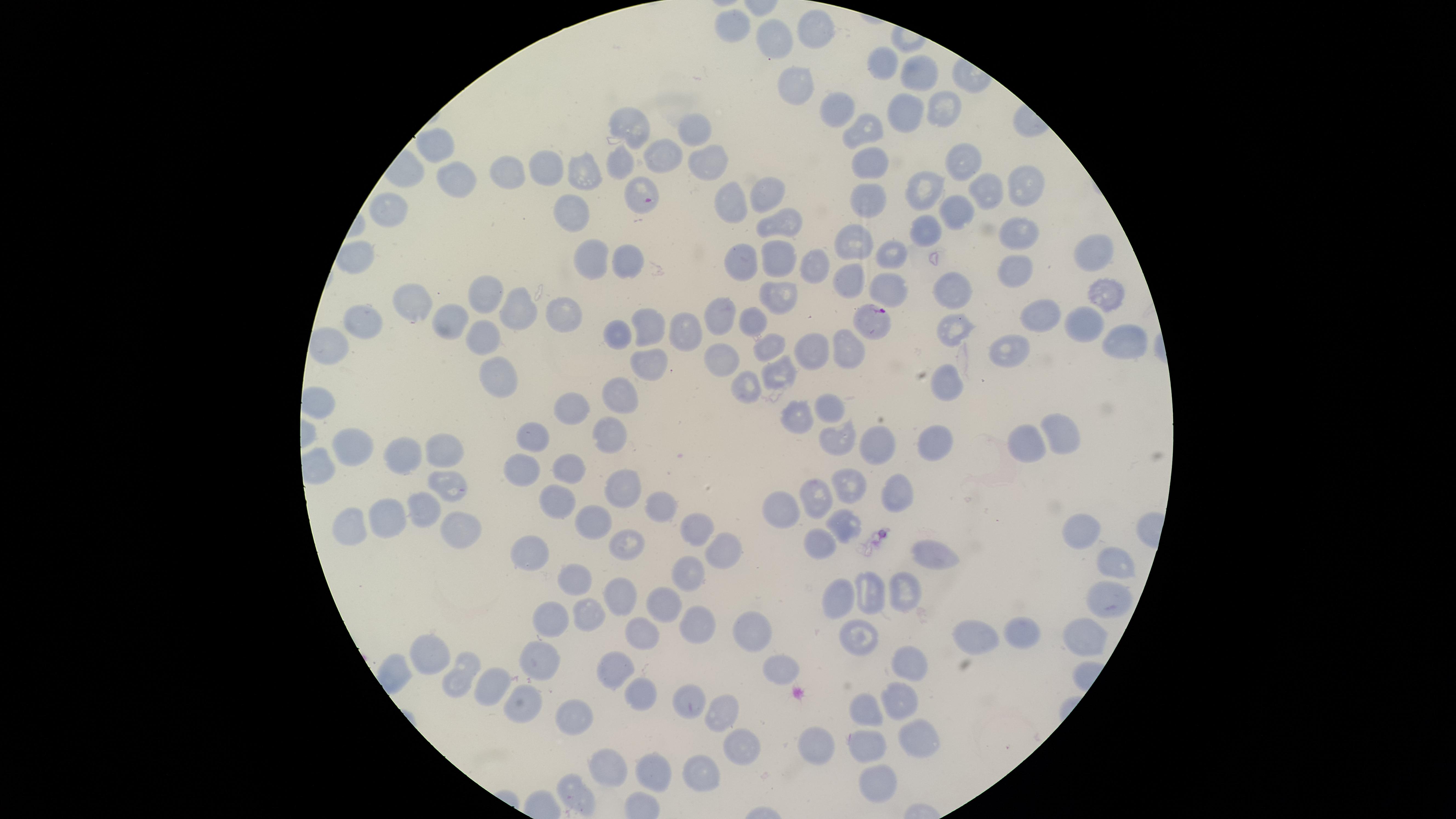

Approximate marker points, in pixels from the top-left corner.
Summary:
  - Parasitized red blood cells: (x=641, y=191), (x=877, y=320)
  - Uninfected red blood cells: (x=735, y=23), (x=813, y=27), (x=776, y=38), (x=884, y=60), (x=922, y=73), (x=797, y=87), (x=909, y=106), (x=840, y=107), (x=946, y=107), (x=632, y=124), (x=867, y=126), (x=692, y=129), (x=431, y=145), (x=666, y=155), (x=967, y=159), (x=707, y=160), (x=873, y=163), (x=622, y=164), (x=546, y=169), (x=583, y=169), (x=506, y=172), (x=446, y=176), (x=1028, y=178), (x=922, y=186), (x=768, y=188), (x=982, y=192), (x=732, y=197), (x=867, y=199), (x=386, y=208), (x=956, y=210), (x=570, y=211), (x=785, y=222), (x=926, y=226), (x=1017, y=229), (x=856, y=241), (x=1091, y=248), (x=779, y=254), (x=892, y=254), (x=590, y=255), (x=748, y=258), (x=814, y=259), (x=624, y=262), (x=1016, y=266), (x=849, y=279), (x=891, y=286), (x=951, y=287), (x=1107, y=287), (x=484, y=290), (x=783, y=294), (x=413, y=300), (x=513, y=305), (x=562, y=313), (x=1036, y=315), (x=363, y=319), (x=1077, y=319), (x=722, y=320), (x=447, y=321), (x=755, y=323), (x=951, y=324), (x=648, y=325), (x=486, y=331), (x=616, y=333), (x=683, y=334), (x=1119, y=334), (x=1005, y=342), (x=775, y=343), (x=808, y=344), (x=853, y=352), (x=722, y=355), (x=653, y=363), (x=497, y=370), (x=777, y=371), (x=741, y=382), (x=949, y=384), (x=620, y=397), (x=577, y=406), (x=828, y=409), (x=796, y=415), (x=1063, y=427), (x=614, y=433), (x=1024, y=437), (x=536, y=439), (x=840, y=439), (x=880, y=441), (x=932, y=441), (x=357, y=445), (x=446, y=450), (x=407, y=452), (x=568, y=463), (x=521, y=466), (x=447, y=485), (x=621, y=485), (x=851, y=485), (x=895, y=493), (x=559, y=497), (x=814, y=499), (x=660, y=502), (x=419, y=504), (x=784, y=507), (x=382, y=514), (x=845, y=521), (x=344, y=522), (x=1081, y=523), (x=588, y=524), (x=455, y=527), (x=699, y=527), (x=630, y=539), (x=821, y=540), (x=723, y=541), (x=533, y=551), (x=933, y=551), (x=1114, y=561), (x=688, y=568), (x=573, y=575), (x=870, y=587), (x=902, y=590), (x=617, y=592), (x=840, y=593), (x=1106, y=598), (x=669, y=600), (x=591, y=611), (x=549, y=614), (x=696, y=617), (x=639, y=630), (x=1022, y=630), (x=753, y=631), (x=1087, y=633), (x=853, y=634), (x=977, y=638), (x=435, y=655), (x=536, y=657), (x=911, y=661), (x=782, y=664), (x=620, y=668), (x=462, y=673), (x=492, y=683), (x=521, y=695), (x=637, y=699), (x=686, y=700), (x=892, y=701), (x=862, y=706), (x=570, y=711), (x=719, y=712), (x=823, y=736), (x=913, y=737), (x=742, y=744), (x=862, y=745), (x=698, y=768), (x=606, y=769), (x=648, y=774), (x=873, y=775), (x=574, y=795)
  - Stain: Giemsa
  - Field of view: single
  - Species: Plasmodium falciparum
  - Preparation: thin blood film
  - Capture: smartphone photograph through the microscope eyepiece
  - Image size: 1456×819 pixels
  - Presence: malaria parasites identified
  - Visible region: circular